Assess this cell for malaria.
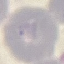

It is uninfected.

Thin blood film. Automatically extracted cell patch, resized to 64 × 64 pixels. Giemsa stain. Acquired by smartphone through the microscope eyepiece.